Assess the morphology of the erythrocytes.
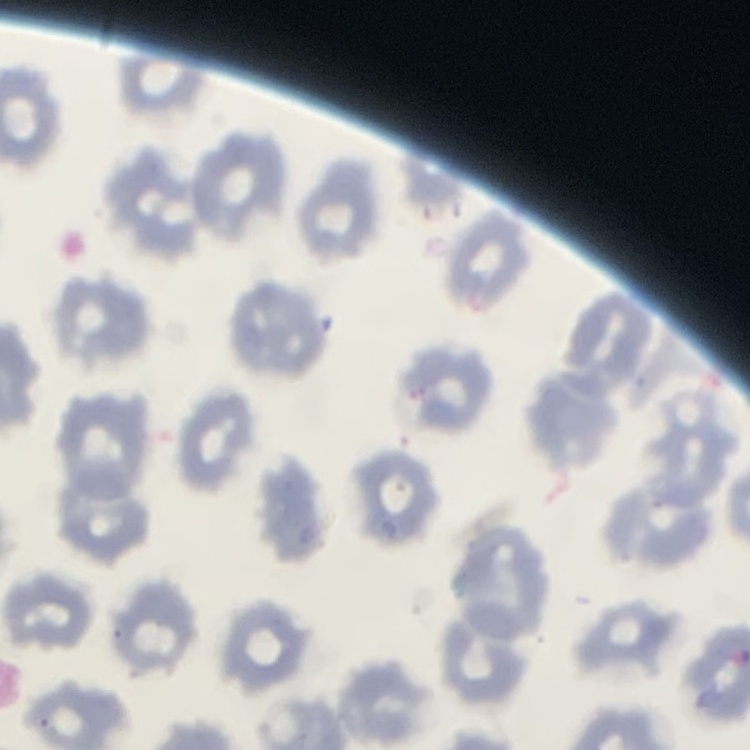
No rouleaux formation.

Stained with either Field's or Giemsa. One tile cut from a larger photomicrograph. Thin blood film.